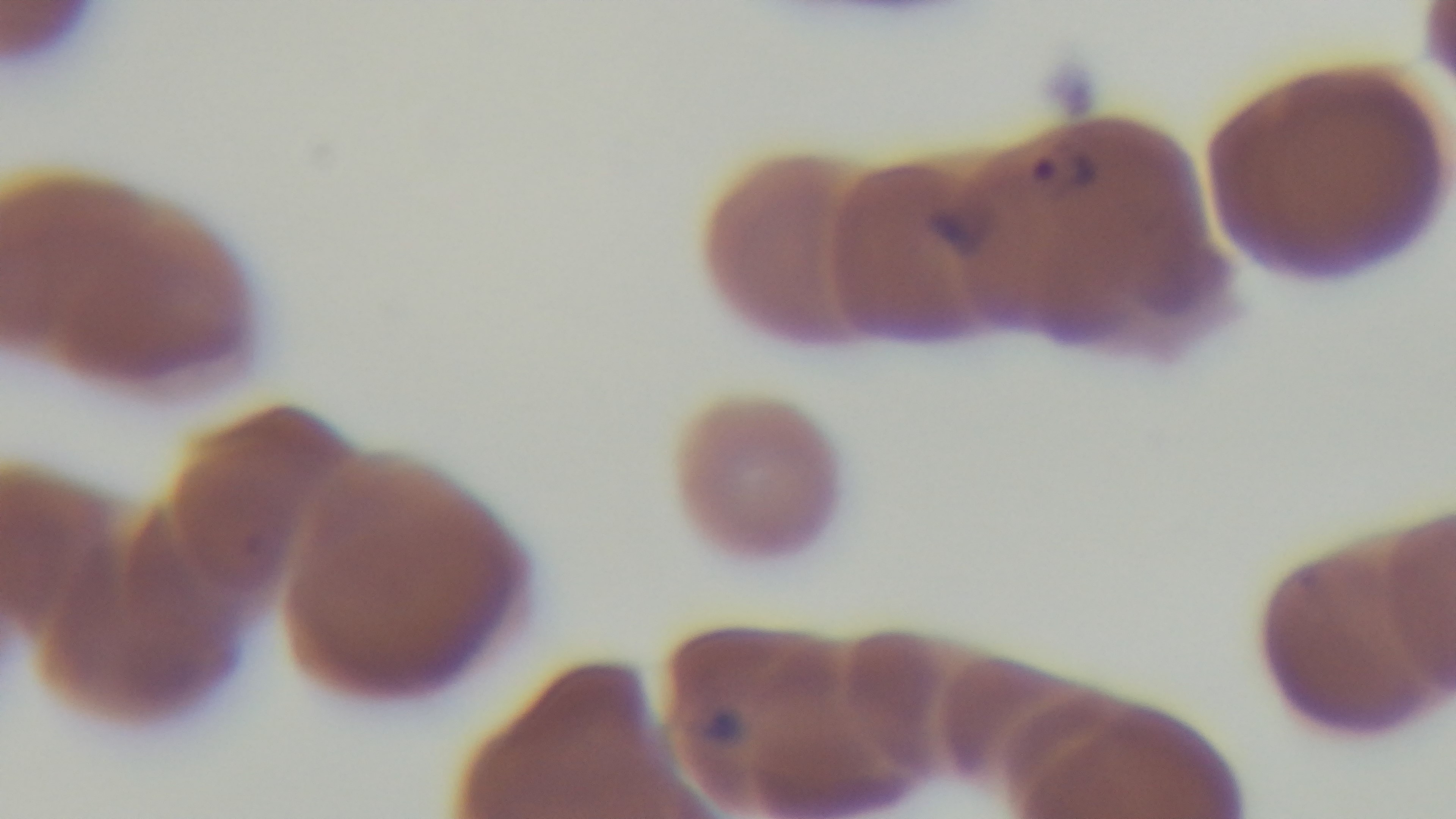
{
  "objective": "100x oil immersion",
  "capture": "mounted 4K digital camera",
  "field_of_view": "single",
  "malaria_status": "infected",
  "preparation": "thin blood film",
  "modality": "light microscopy",
  "stain": "Giemsa"
}